Give the extent of all uninfected red blood cells.
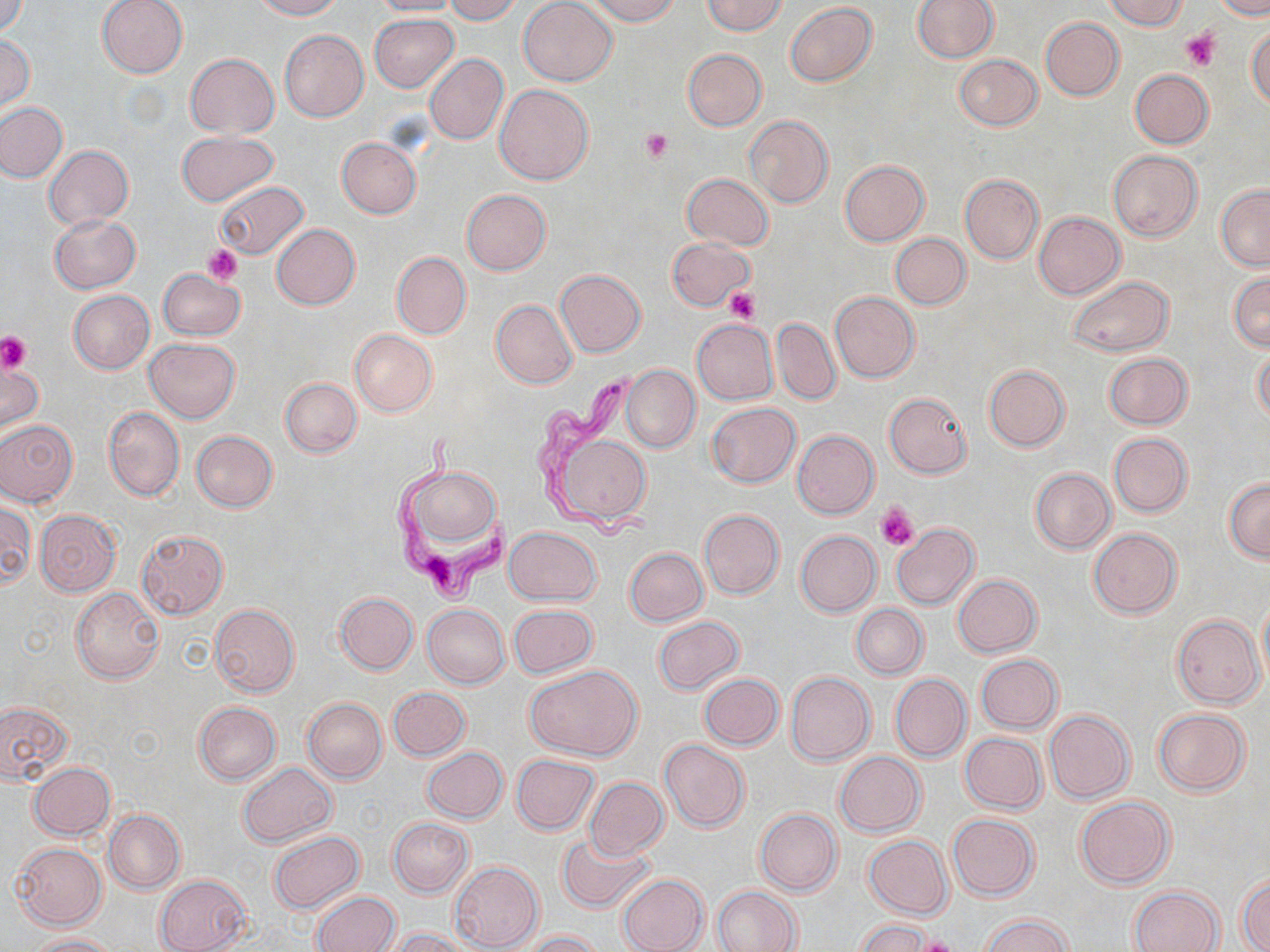

Approximate bounding boxes as named x1/y1/x2/y2 corners in pixels.
Uninfected red blood cells: (x1=1, y1=0, x2=28, y2=37), (x1=96, y1=0, x2=188, y2=78), (x1=248, y1=0, x2=343, y2=20), (x1=369, y1=0, x2=465, y2=17), (x1=443, y1=0, x2=521, y2=24), (x1=519, y1=0, x2=617, y2=86), (x1=585, y1=0, x2=680, y2=25), (x1=702, y1=0, x2=789, y2=35), (x1=912, y1=0, x2=999, y2=62), (x1=1102, y1=0, x2=1190, y2=30), (x1=1214, y1=0, x2=1269, y2=19), (x1=784, y1=3, x2=877, y2=86), (x1=369, y1=13, x2=459, y2=92), (x1=1041, y1=17, x2=1125, y2=100), (x1=1247, y1=27, x2=1270, y2=109), (x1=279, y1=29, x2=368, y2=122), (x1=0, y1=34, x2=35, y2=111), (x1=682, y1=49, x2=767, y2=131), (x1=185, y1=53, x2=279, y2=137), (x1=424, y1=53, x2=508, y2=146), (x1=954, y1=54, x2=1041, y2=130), (x1=1130, y1=69, x2=1213, y2=148), (x1=495, y1=84, x2=594, y2=185), (x1=0, y1=102, x2=66, y2=183), (x1=743, y1=115, x2=833, y2=209), (x1=177, y1=131, x2=278, y2=207), (x1=337, y1=137, x2=421, y2=219), (x1=44, y1=145, x2=133, y2=230), (x1=1108, y1=150, x2=1202, y2=242), (x1=840, y1=160, x2=929, y2=245), (x1=681, y1=174, x2=773, y2=250), (x1=960, y1=175, x2=1044, y2=263), (x1=214, y1=183, x2=308, y2=261), (x1=1216, y1=185, x2=1270, y2=271), (x1=461, y1=190, x2=551, y2=276), (x1=1033, y1=212, x2=1125, y2=299), (x1=49, y1=213, x2=141, y2=293), (x1=271, y1=223, x2=360, y2=310), (x1=891, y1=233, x2=970, y2=310), (x1=667, y1=237, x2=753, y2=311), (x1=392, y1=252, x2=471, y2=338), (x1=157, y1=269, x2=245, y2=340), (x1=554, y1=270, x2=645, y2=357), (x1=1228, y1=271, x2=1269, y2=351), (x1=1066, y1=276, x2=1173, y2=357), (x1=68, y1=290, x2=155, y2=374), (x1=831, y1=291, x2=919, y2=383), (x1=491, y1=300, x2=578, y2=388), (x1=770, y1=318, x2=840, y2=404), (x1=691, y1=319, x2=778, y2=404), (x1=350, y1=330, x2=437, y2=417), (x1=145, y1=338, x2=240, y2=423), (x1=1252, y1=347, x2=1270, y2=426), (x1=1103, y1=352, x2=1192, y2=430), (x1=0, y1=359, x2=42, y2=434), (x1=621, y1=365, x2=699, y2=452), (x1=984, y1=365, x2=1069, y2=451), (x1=279, y1=377, x2=362, y2=458), (x1=883, y1=392, x2=972, y2=478), (x1=707, y1=403, x2=801, y2=487), (x1=104, y1=406, x2=185, y2=502), (x1=0, y1=420, x2=78, y2=507), (x1=547, y1=429, x2=654, y2=529), (x1=191, y1=431, x2=277, y2=512), (x1=792, y1=431, x2=879, y2=518), (x1=1108, y1=432, x2=1192, y2=517), (x1=402, y1=465, x2=501, y2=551), (x1=1030, y1=468, x2=1116, y2=553), (x1=1225, y1=477, x2=1270, y2=562), (x1=0, y1=502, x2=34, y2=589), (x1=35, y1=509, x2=121, y2=596), (x1=700, y1=509, x2=784, y2=599), (x1=891, y1=524, x2=980, y2=609), (x1=505, y1=527, x2=600, y2=605), (x1=1088, y1=528, x2=1182, y2=618), (x1=135, y1=530, x2=230, y2=620), (x1=795, y1=530, x2=880, y2=616), (x1=625, y1=547, x2=708, y2=626), (x1=953, y1=574, x2=1041, y2=657), (x1=71, y1=587, x2=165, y2=684), (x1=335, y1=592, x2=418, y2=674), (x1=1257, y1=594, x2=1270, y2=689), (x1=851, y1=603, x2=927, y2=679), (x1=209, y1=604, x2=299, y2=696), (x1=422, y1=604, x2=509, y2=688), (x1=508, y1=605, x2=597, y2=678), (x1=1172, y1=615, x2=1264, y2=707), (x1=653, y1=617, x2=744, y2=695), (x1=976, y1=654, x2=1063, y2=733), (x1=525, y1=664, x2=642, y2=761), (x1=785, y1=671, x2=875, y2=765), (x1=699, y1=673, x2=784, y2=750), (x1=890, y1=674, x2=970, y2=761), (x1=388, y1=687, x2=470, y2=761), (x1=303, y1=698, x2=387, y2=784), (x1=0, y1=700, x2=72, y2=783), (x1=194, y1=701, x2=281, y2=785), (x1=1151, y1=708, x2=1251, y2=796), (x1=1044, y1=710, x2=1134, y2=803), (x1=961, y1=732, x2=1046, y2=813), (x1=660, y1=740, x2=749, y2=832), (x1=422, y1=748, x2=507, y2=823), (x1=834, y1=751, x2=926, y2=836), (x1=511, y1=754, x2=599, y2=833), (x1=28, y1=762, x2=115, y2=840), (x1=238, y1=763, x2=337, y2=848), (x1=583, y1=777, x2=668, y2=861), (x1=1076, y1=796, x2=1175, y2=889), (x1=755, y1=809, x2=841, y2=896), (x1=105, y1=810, x2=184, y2=894), (x1=946, y1=814, x2=1039, y2=900), (x1=388, y1=818, x2=473, y2=896), (x1=269, y1=831, x2=364, y2=914), (x1=555, y1=832, x2=658, y2=916), (x1=864, y1=835, x2=952, y2=919), (x1=10, y1=842, x2=107, y2=930), (x1=449, y1=861, x2=543, y2=952), (x1=1236, y1=872, x2=1270, y2=952), (x1=154, y1=874, x2=250, y2=952), (x1=616, y1=874, x2=709, y2=952), (x1=711, y1=886, x2=800, y2=952), (x1=1128, y1=886, x2=1223, y2=952), (x1=312, y1=892, x2=399, y2=952), (x1=979, y1=913, x2=1075, y2=952), (x1=855, y1=920, x2=932, y2=952), (x1=388, y1=928, x2=476, y2=952), (x1=521, y1=930, x2=604, y2=951), (x1=26, y1=934, x2=117, y2=952).

Summary:
  - Trypanosoma brucei locations: (x1=524, y1=369, x2=665, y2=544), (x1=389, y1=432, x2=512, y2=605)
  - Platelet locations: (x1=1180, y1=29, x2=1221, y2=72), (x1=640, y1=129, x2=672, y2=162), (x1=201, y1=244, x2=243, y2=284), (x1=721, y1=287, x2=761, y2=325), (x1=0, y1=331, x2=32, y2=373), (x1=875, y1=503, x2=920, y2=551), (x1=915, y1=936, x2=959, y2=952)
  - Slide-level diagnosis: Trypanosoma brucei
  - Field of view: single
  - Image size: 1270×952 pixels
  - Stain: May-Grünwald-Giemsa
  - Modality: light microscopy
  - Magnification: 1000x
  - Preparation: thin blood smear